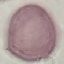

Summary:
  - Result: no malaria parasites detected
  - Preparation: thin smear
  - Stain: Giemsa
  - Image type: cell patch, automatically extracted from a larger field of view and resized to 64 × 64 pixels
  - Capture: smartphone camera at the microscope eyepiece